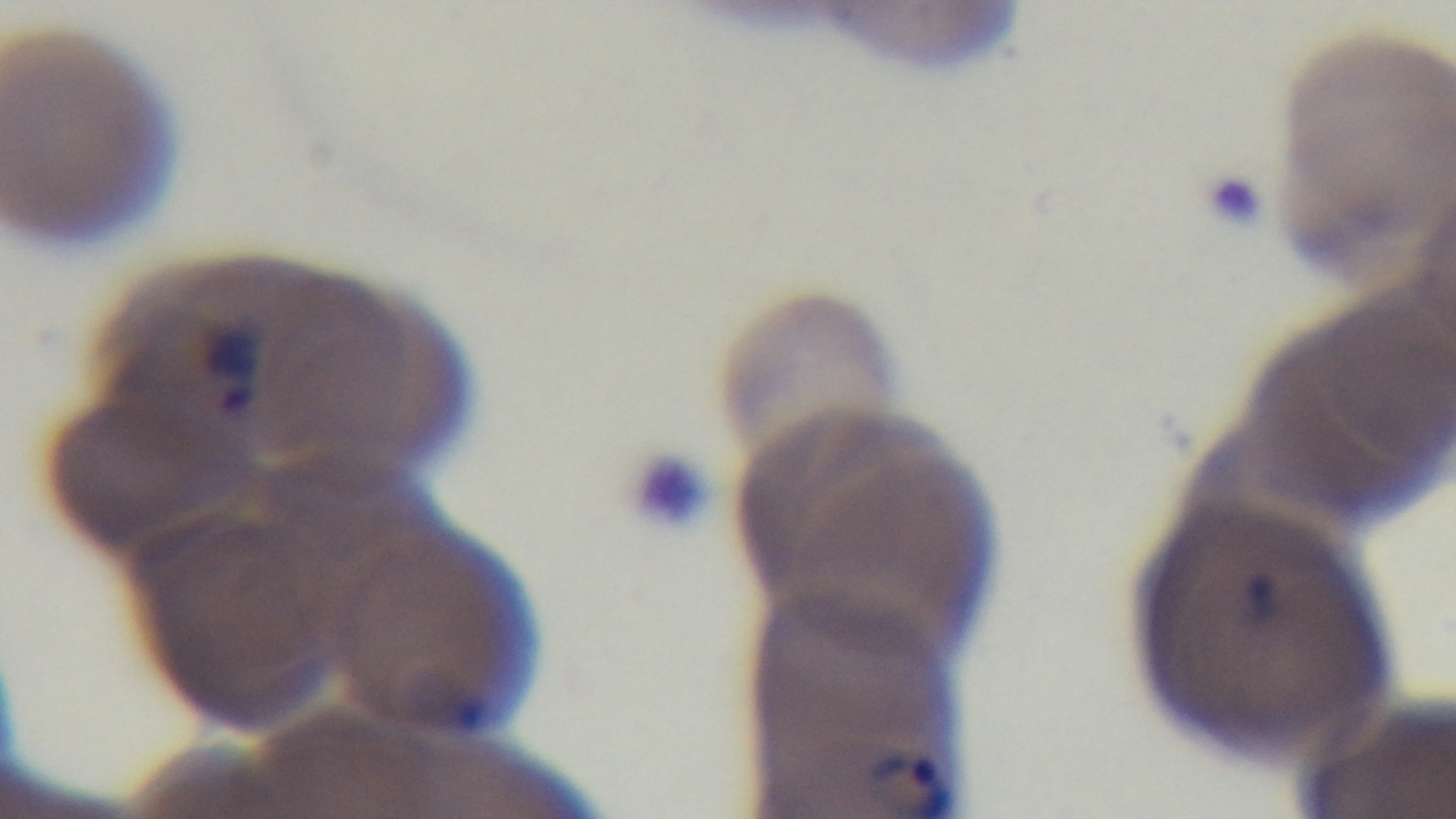 Photomicrograph. Single field of view. Preparation: thin smear. Giemsa stain. Captured with a mounted 4K digital camera. Malaria status: positive. 100x oil-immersion objective.